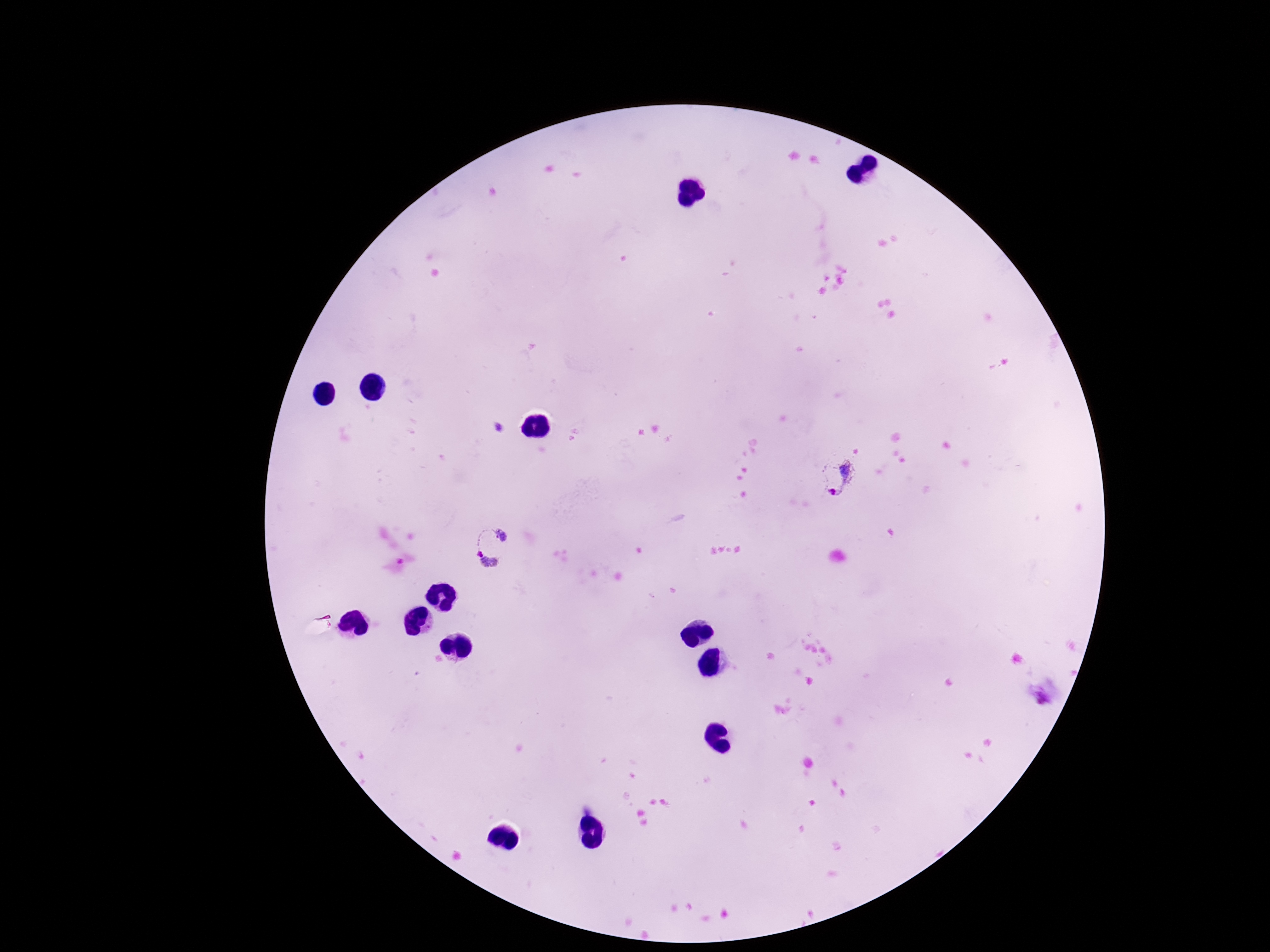

{
  "field_of_view": "one from this slide",
  "preparation": "thick peripheral-blood smear",
  "magnification": "100x",
  "plasmodium_parasite_locations": "approximate object centers, in pixels from the top-left corner: (x=836, y=477), (x=493, y=546)",
  "stain": "Giemsa",
  "patient_malaria_status": "positive",
  "capture": "smartphone camera through the microscope eyepiece",
  "image_size": "1270×952 pixels"
}